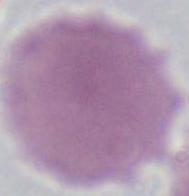

modality = photomicrograph
magnification = 1000x
identification = erythrocyte